Locate every blood parasite and identify its species.
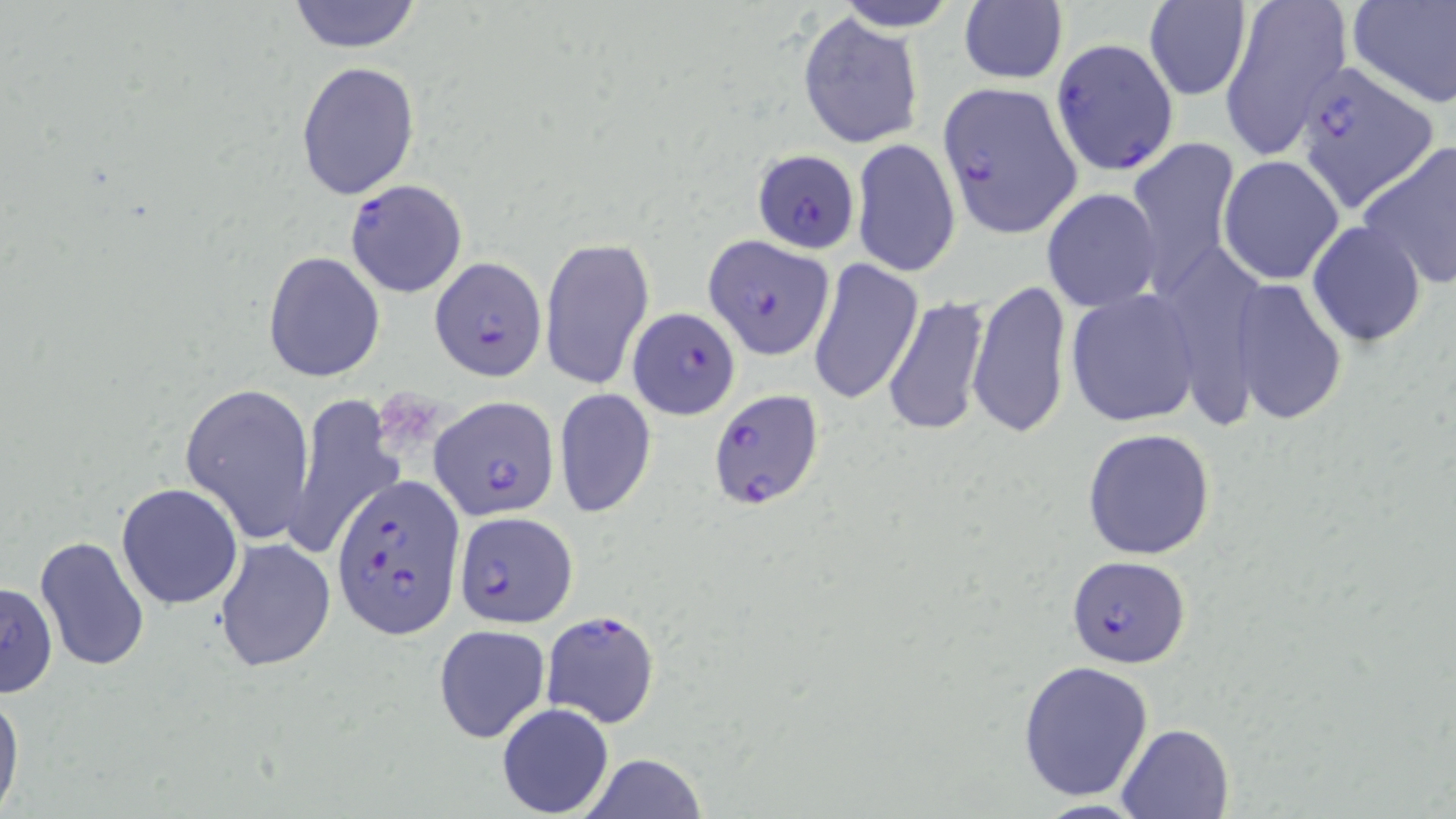
Approximate bounding boxes as (x1,y1)-(x2,y2) corner pairs in pixels.
Plasmodium falciparum-infected red blood cells: (1051,36)-(1178,174), (1297,64)-(1438,210), (937,81)-(1083,240), (752,149)-(860,254), (344,178)-(469,299), (703,230)-(833,360), (430,257)-(548,383), (626,306)-(741,421), (707,390)-(826,511), (432,395)-(557,522), (332,474)-(465,642), (452,509)-(578,628), (1068,557)-(1193,669), (540,609)-(661,729).
No Plasmodium ovale, Plasmodium malariae, Plasmodium vivax, Babesia divergens, or Trypanosoma brucei observed.

Summary:
  - Uninfected red blood cell locations: (286,0)-(424,53), (829,0)-(963,30), (1216,0)-(1352,157), (1348,0)-(1456,110), (959,2)-(1068,86), (1143,2)-(1254,101), (798,12)-(925,148), (294,62)-(420,199), (1126,138)-(1240,295), (850,139)-(960,276), (1357,142)-(1456,293), (1218,155)-(1345,283), (1041,187)-(1162,313), (1307,221)-(1427,348), (539,235)-(655,391), (263,251)-(386,381), (808,258)-(924,406), (965,280)-(1073,439), (1233,283)-(1348,423), (1065,291)-(1202,427), (883,295)-(990,435), (179,382)-(316,545), (553,389)-(656,518), (284,392)-(401,564), (1083,427)-(1216,560), (115,482)-(244,610), (33,535)-(153,672), (214,538)-(337,673), (0,581)-(58,698), (433,625)-(551,744), (1016,659)-(1154,802), (1,687)-(24,819), (496,702)-(614,816), (1115,722)-(1237,818), (579,753)-(708,818)
  - Platelet locations: (373,387)-(445,452)
  - Slide-level diagnosis: Plasmodium falciparum
  - Field of view: one of a larger specimen
  - Image size: 1456×819 pixels
  - Modality: optical microscopy
  - Stain: May-Grünwald-Giemsa
  - Preparation: thin blood film
  - Magnification: 1000x